State which parasite is depicted.
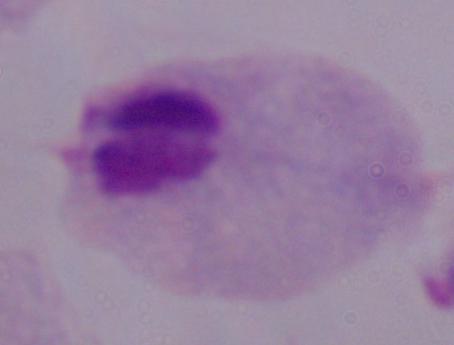
A trichomonad.

Summary:
  - Magnification: 1000x
  - Modality: micrograph